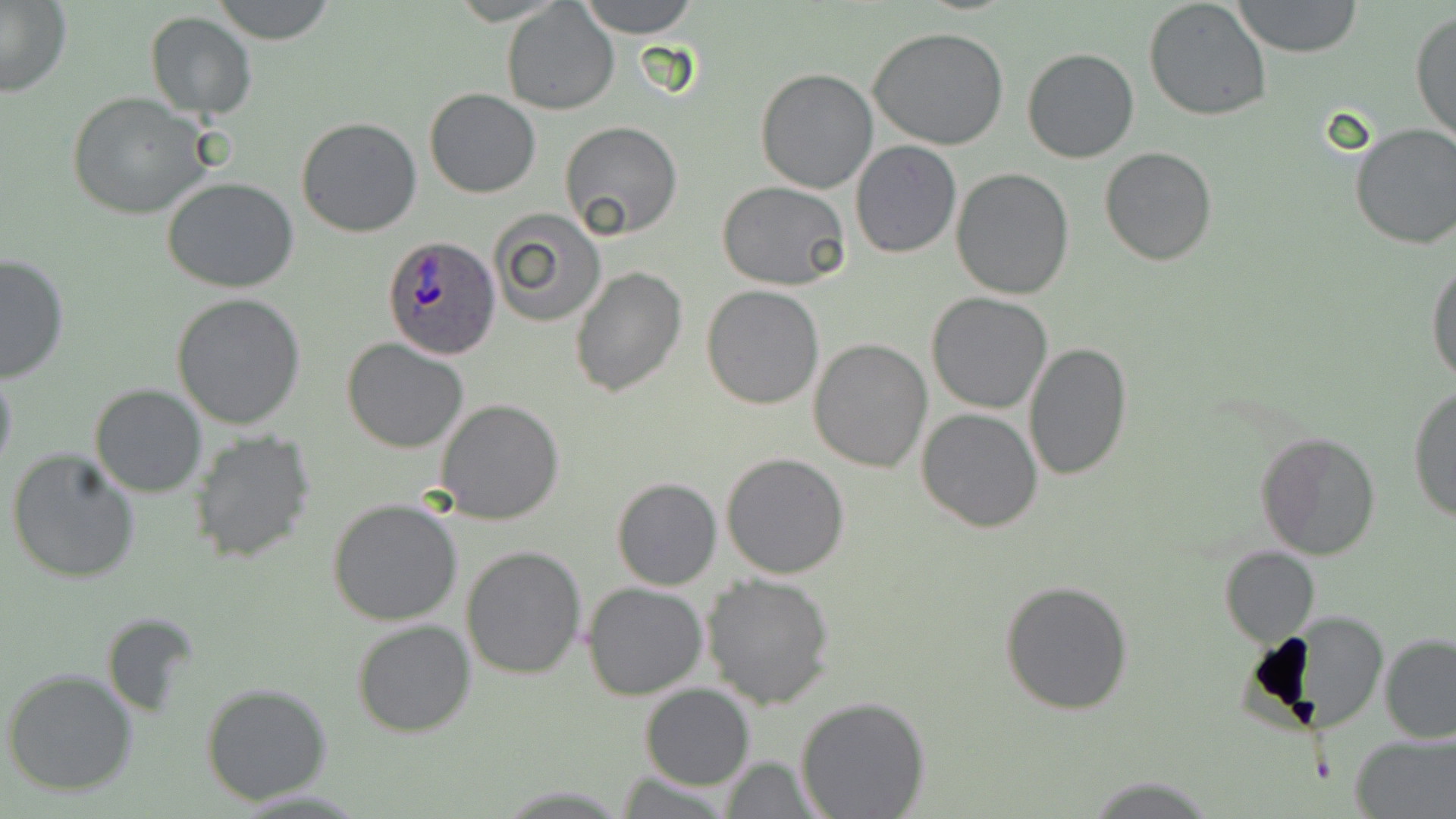
Approximate bounding boxes as [x1, y1, x2, y2] in pixels. Plasmodium ovale-infected red blood cell locations: [381, 236, 501, 361]. Uninfected red blood cell locations: [214, 0, 339, 45], [580, 0, 699, 39], [1233, 0, 1363, 57], [1143, 1, 1273, 120], [0, 2, 73, 97], [502, 2, 619, 117], [1410, 7, 1456, 147], [145, 11, 256, 119], [867, 26, 1010, 151], [1022, 47, 1140, 163], [755, 68, 879, 194], [424, 88, 541, 198], [67, 91, 211, 219], [296, 117, 423, 237], [561, 121, 682, 241], [1348, 124, 1456, 250], [850, 140, 962, 258], [1099, 145, 1217, 265], [951, 168, 1075, 299], [162, 177, 299, 293], [719, 181, 852, 290], [491, 210, 605, 327], [0, 252, 70, 384], [1427, 256, 1456, 385], [569, 265, 687, 398], [701, 284, 823, 409], [927, 292, 1054, 412], [173, 293, 307, 429], [807, 338, 932, 472], [342, 339, 469, 454], [1024, 343, 1133, 482], [0, 364, 19, 488], [90, 385, 207, 498], [1409, 386, 1455, 523], [436, 397, 565, 523], [916, 408, 1043, 533], [1257, 430, 1382, 559], [187, 431, 317, 564], [6, 447, 141, 585], [720, 451, 850, 577], [612, 477, 722, 590], [326, 497, 464, 627], [461, 546, 587, 680], [1219, 546, 1319, 645], [701, 572, 838, 710], [998, 580, 1136, 717], [581, 581, 708, 699], [102, 611, 200, 720], [1270, 613, 1392, 734], [352, 620, 477, 736], [1379, 634, 1456, 743], [3, 669, 137, 796], [200, 682, 332, 805], [640, 683, 756, 790], [795, 697, 931, 818], [1351, 732, 1455, 817], [718, 757, 827, 816], [1086, 776, 1217, 816]. Slide-level diagnosis: Plasmodium ovale. Captured at 1000x magnification. May-Grünwald-Giemsa-stained preparation. Thin blood film. Single field of view. Image is 1456×819 pixels. Optical microscopy.